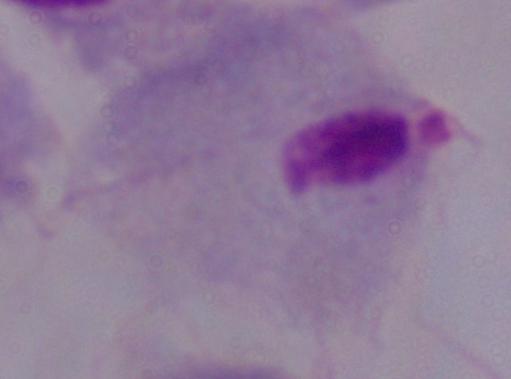

Summary:
  - Modality: micrograph
  - Magnification: 1000x
  - Identification: trichomonad